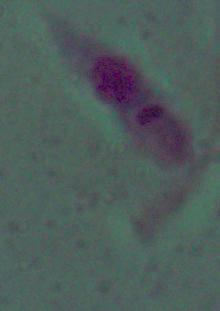

modality = micrograph
magnification = 1000x
identification = Leishmania